Comment on the morphology of the erythrocytes.
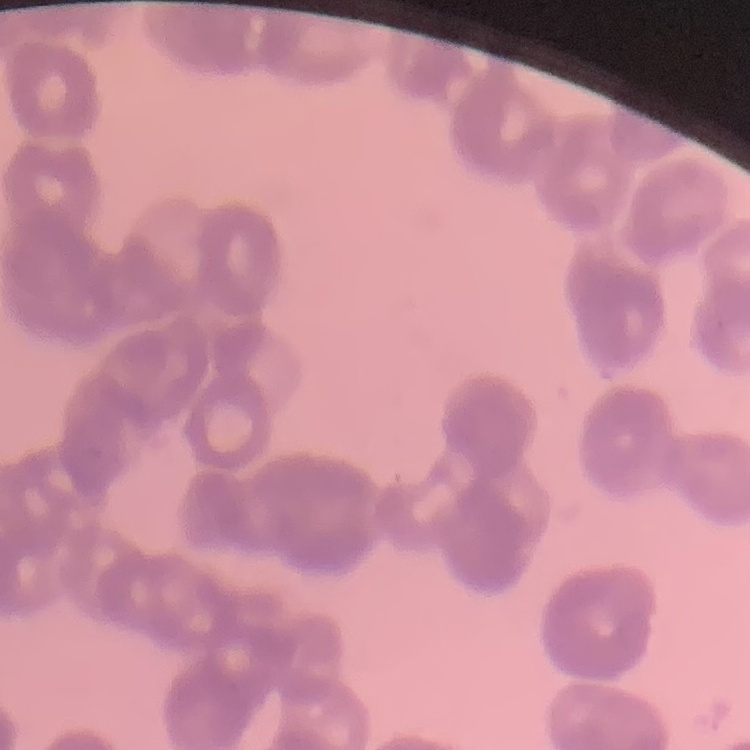
They show rouleaux formation.

Stained with either Field's or Giemsa. Thin peripheral smear. One tile cut from a larger photomicrograph.